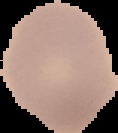
image size = 118×133 pixels
malaria status = uninfected
image type = segmented cell region with the area outside set to black
preparation = thin blood smear